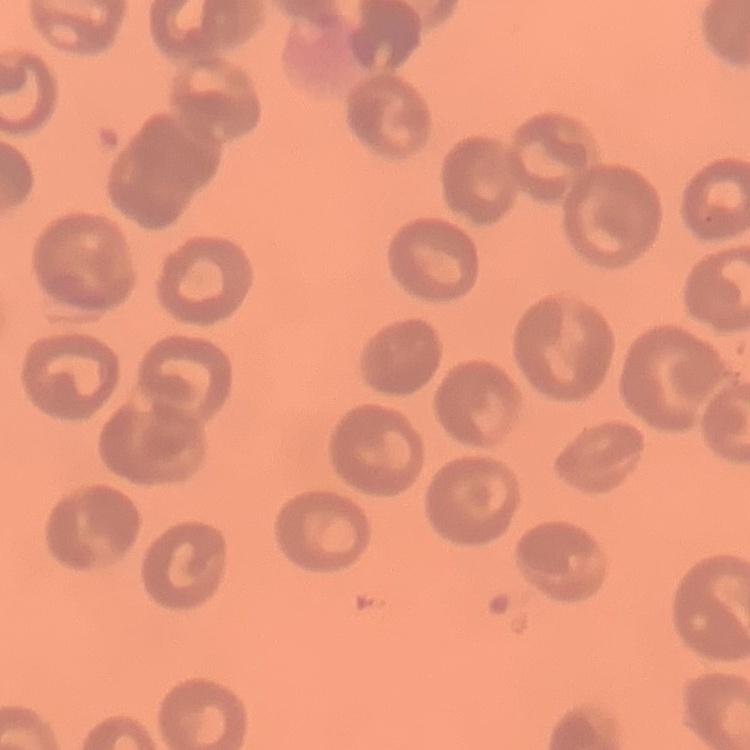

{
  "erythrocyte_morphology": "no rouleaux formation",
  "image_type": "one tile cut from a larger photomicrograph",
  "preparation": "thin blood smear",
  "stain": "Field's or Giemsa"
}